State the blood parasite species.
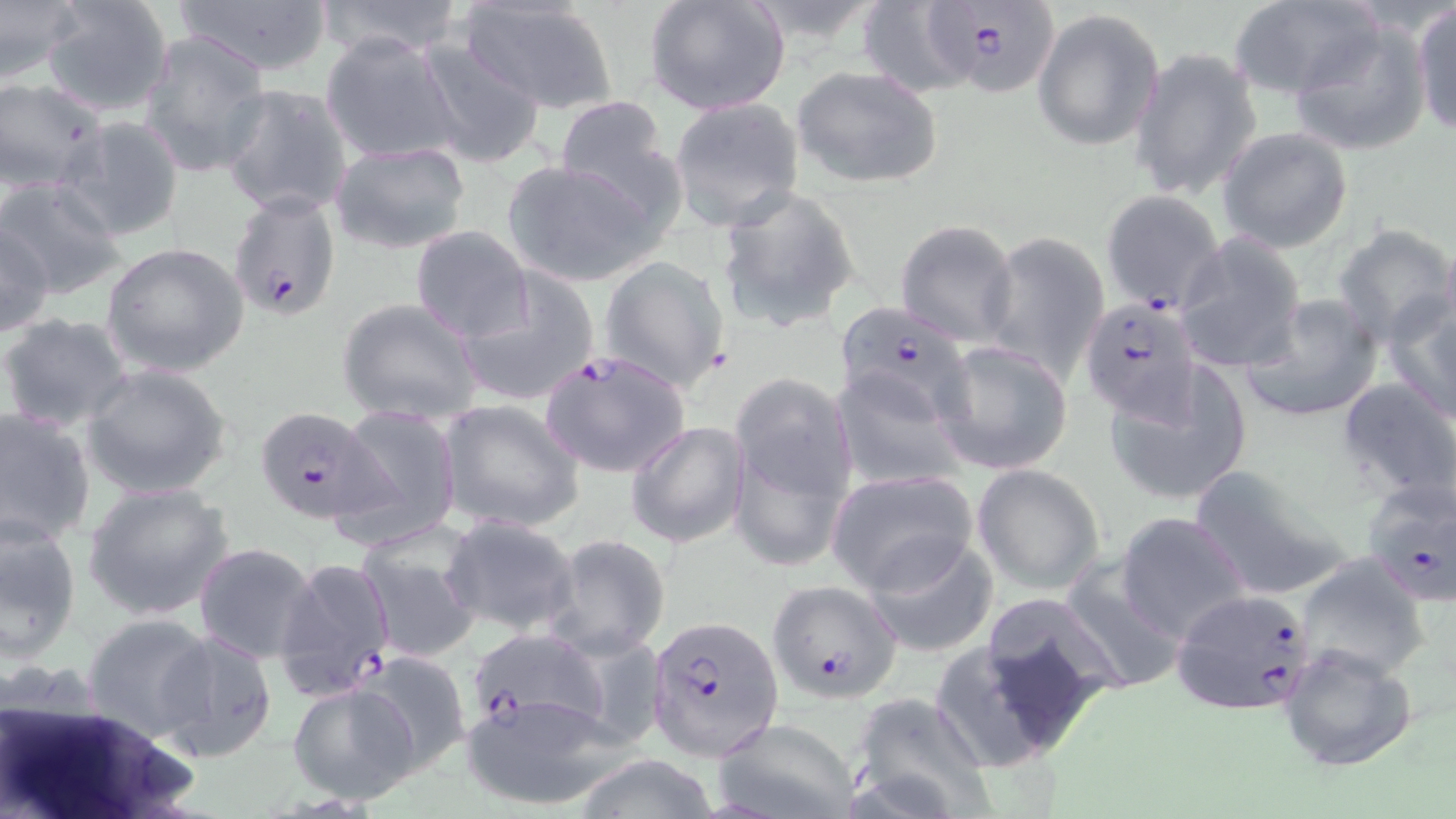
Plasmodium falciparum.

Summary:
  - Coordinate format: approximate bounding boxes as named x1/y1/x2/y2 corners in pixels
  - Uninfected red blood cell locations (subset): (x1=0, y1=0, x2=84, y2=87), (x1=39, y1=0, x2=176, y2=116), (x1=166, y1=0, x2=337, y2=78), (x1=314, y1=0, x2=465, y2=61), (x1=457, y1=0, x2=619, y2=115), (x1=644, y1=0, x2=791, y2=117), (x1=1228, y1=0, x2=1379, y2=98), (x1=856, y1=1, x2=986, y2=97), (x1=1411, y1=3, x2=1456, y2=138), (x1=1031, y1=8, x2=1164, y2=152), (x1=1287, y1=20, x2=1434, y2=158), (x1=138, y1=30, x2=271, y2=180), (x1=320, y1=33, x2=462, y2=166), (x1=415, y1=37, x2=550, y2=168), (x1=1131, y1=48, x2=1260, y2=203), (x1=790, y1=65, x2=944, y2=190), (x1=0, y1=78, x2=107, y2=192), (x1=220, y1=83, x2=354, y2=217), (x1=552, y1=95, x2=688, y2=229), (x1=668, y1=97, x2=805, y2=230), (x1=63, y1=115, x2=184, y2=242), (x1=1218, y1=127, x2=1353, y2=253), (x1=328, y1=141, x2=471, y2=254), (x1=501, y1=157, x2=661, y2=288), (x1=0, y1=176, x2=129, y2=299), (x1=713, y1=183, x2=865, y2=332), (x1=894, y1=219, x2=1020, y2=343), (x1=1, y1=221, x2=56, y2=339), (x1=1333, y1=222, x2=1456, y2=348), (x1=410, y1=226, x2=534, y2=343), (x1=1175, y1=233, x2=1307, y2=372), (x1=983, y1=234, x2=1110, y2=383), (x1=101, y1=241, x2=249, y2=379), (x1=598, y1=255, x2=730, y2=390), (x1=456, y1=270, x2=601, y2=407), (x1=1382, y1=287, x2=1456, y2=424), (x1=1241, y1=293, x2=1383, y2=424), (x1=337, y1=298, x2=481, y2=425), (x1=0, y1=312, x2=135, y2=434), (x1=934, y1=339, x2=1074, y2=475), (x1=80, y1=363, x2=233, y2=499), (x1=1101, y1=367, x2=1249, y2=508), (x1=832, y1=368, x2=964, y2=491), (x1=728, y1=373, x2=859, y2=540), (x1=1337, y1=378, x2=1456, y2=504), (x1=437, y1=399, x2=585, y2=533), (x1=329, y1=403, x2=462, y2=548), (x1=0, y1=407, x2=97, y2=548), (x1=625, y1=421, x2=749, y2=548), (x1=1186, y1=462, x2=1352, y2=598), (x1=972, y1=463, x2=1105, y2=595), (x1=826, y1=470, x2=978, y2=594), (x1=81, y1=480, x2=237, y2=621), (x1=0, y1=511, x2=82, y2=662), (x1=1116, y1=512, x2=1251, y2=645), (x1=440, y1=516, x2=580, y2=637), (x1=355, y1=532, x2=482, y2=662), (x1=861, y1=533, x2=999, y2=658), (x1=542, y1=534, x2=671, y2=660), (x1=194, y1=542, x2=319, y2=665), (x1=1292, y1=552, x2=1433, y2=683), (x1=1057, y1=554, x2=1187, y2=697), (x1=962, y1=597, x2=1127, y2=755), (x1=82, y1=612, x2=216, y2=742), (x1=155, y1=628, x2=278, y2=762), (x1=924, y1=636, x2=1086, y2=777), (x1=1279, y1=642, x2=1419, y2=773), (x1=351, y1=650, x2=473, y2=776), (x1=288, y1=683, x2=420, y2=805), (x1=460, y1=693, x2=620, y2=811), (x1=849, y1=693, x2=998, y2=819), (x1=712, y1=719, x2=859, y2=818), (x1=567, y1=754, x2=725, y2=819)
  - Plasmodium falciparum-infected red blood cell locations (subset): (x1=922, y1=1, x2=1064, y2=103), (x1=1101, y1=189, x2=1228, y2=315), (x1=229, y1=190, x2=342, y2=323), (x1=1079, y1=297, x2=1203, y2=424), (x1=834, y1=300, x2=977, y2=432), (x1=534, y1=347, x2=690, y2=480), (x1=254, y1=406, x2=383, y2=525), (x1=1359, y1=479, x2=1456, y2=610), (x1=274, y1=555, x2=396, y2=701), (x1=1169, y1=587, x2=1318, y2=715), (x1=651, y1=617, x2=783, y2=758), (x1=463, y1=628, x2=609, y2=737)
  - Image size: 1456×819 pixels
  - Modality: light microscopy
  - Preparation: thin blood smear
  - Field of view: single
  - Magnification: 1000x
  - Stain: May-Grünwald-Giemsa